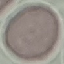
malaria_status: uninfected
stain: Giemsa
image_type: automatically extracted cell patch, resized to 64 × 64 pixels
capture: smartphone camera at the microscope eyepiece
preparation: thin blood smear